Assess the morphology of the red blood cells.
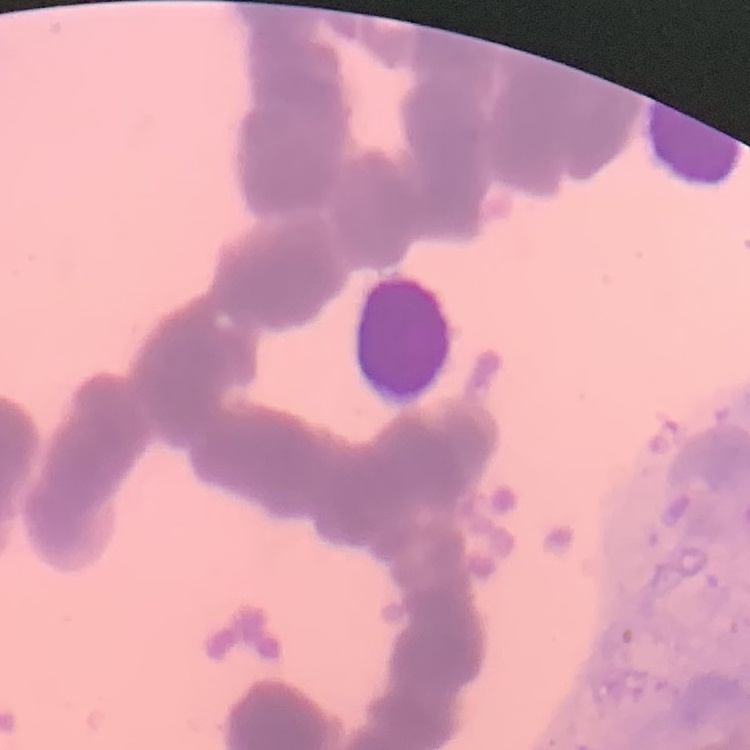
Rouleaux formation.

{
  "preparation": "thin blood film",
  "image_type": "square crop of a larger photomicrograph",
  "stain": "Field's or Giemsa"
}